State which cell type is depicted.
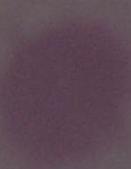
This is an erythrocyte.

{
  "magnification": "1000x",
  "modality": "micrograph"
}